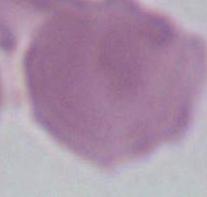

{
  "magnification": "1000x",
  "identification": "erythrocyte",
  "modality": "photomicrograph"
}